Evaluate for malaria.
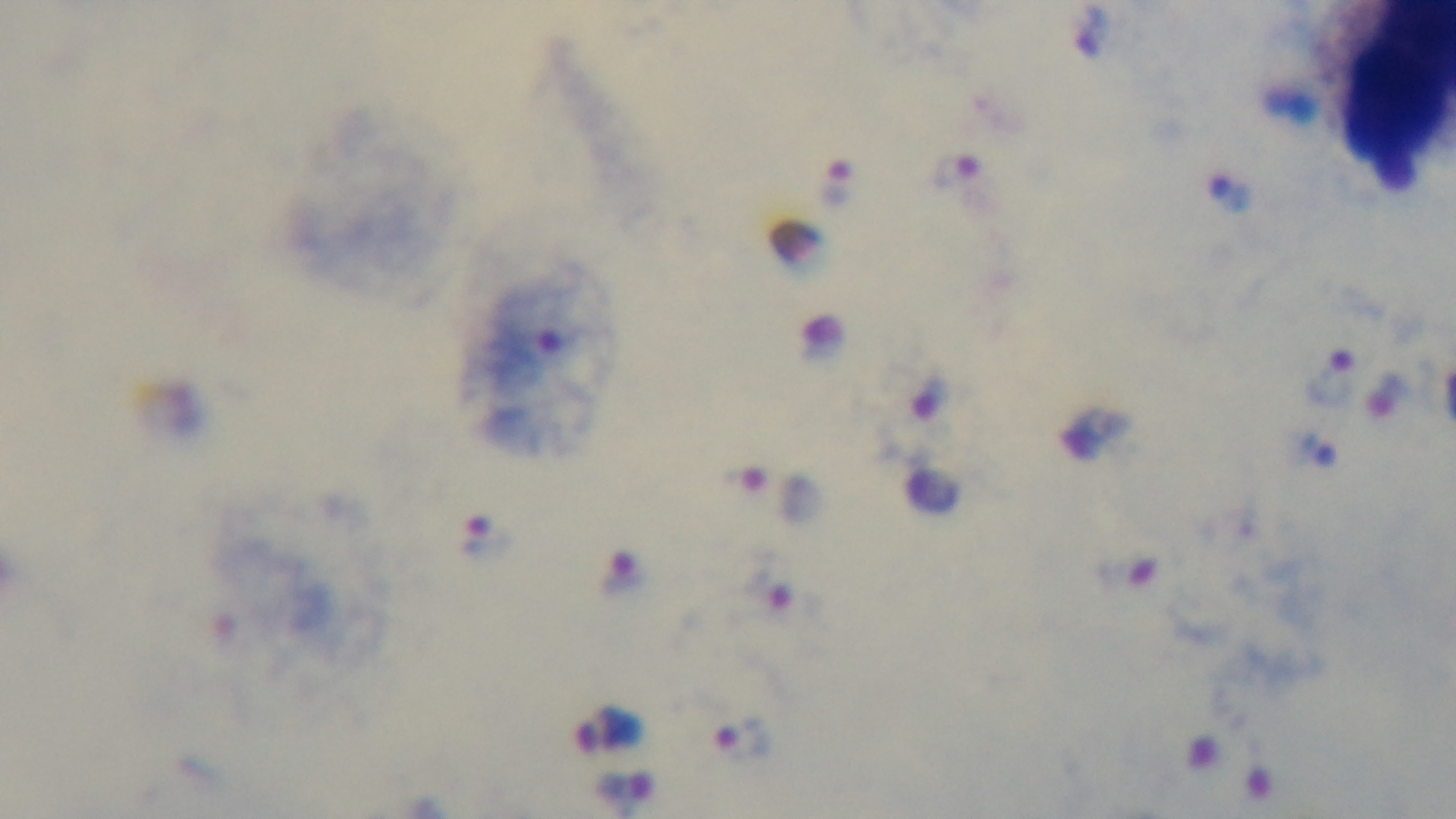

Infected.

Summary:
  - Stain: Giemsa
  - Preparation: thick smear
  - Modality: light microscopy
  - Objective: 100x oil immersion
  - Field of view: one from the slide
  - Capture: mounted 4K digital camera